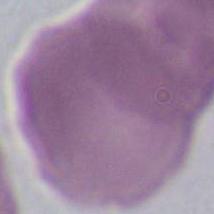

Micrograph. Captured at 1000x magnification. A red blood cell is seen.